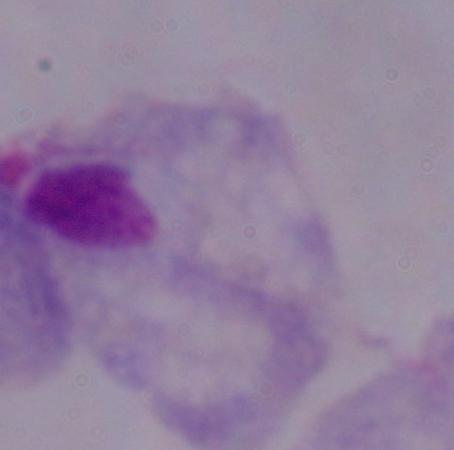
Summary:
  - Identification: trichomonad
  - Magnification: 1000x
  - Modality: photomicrograph